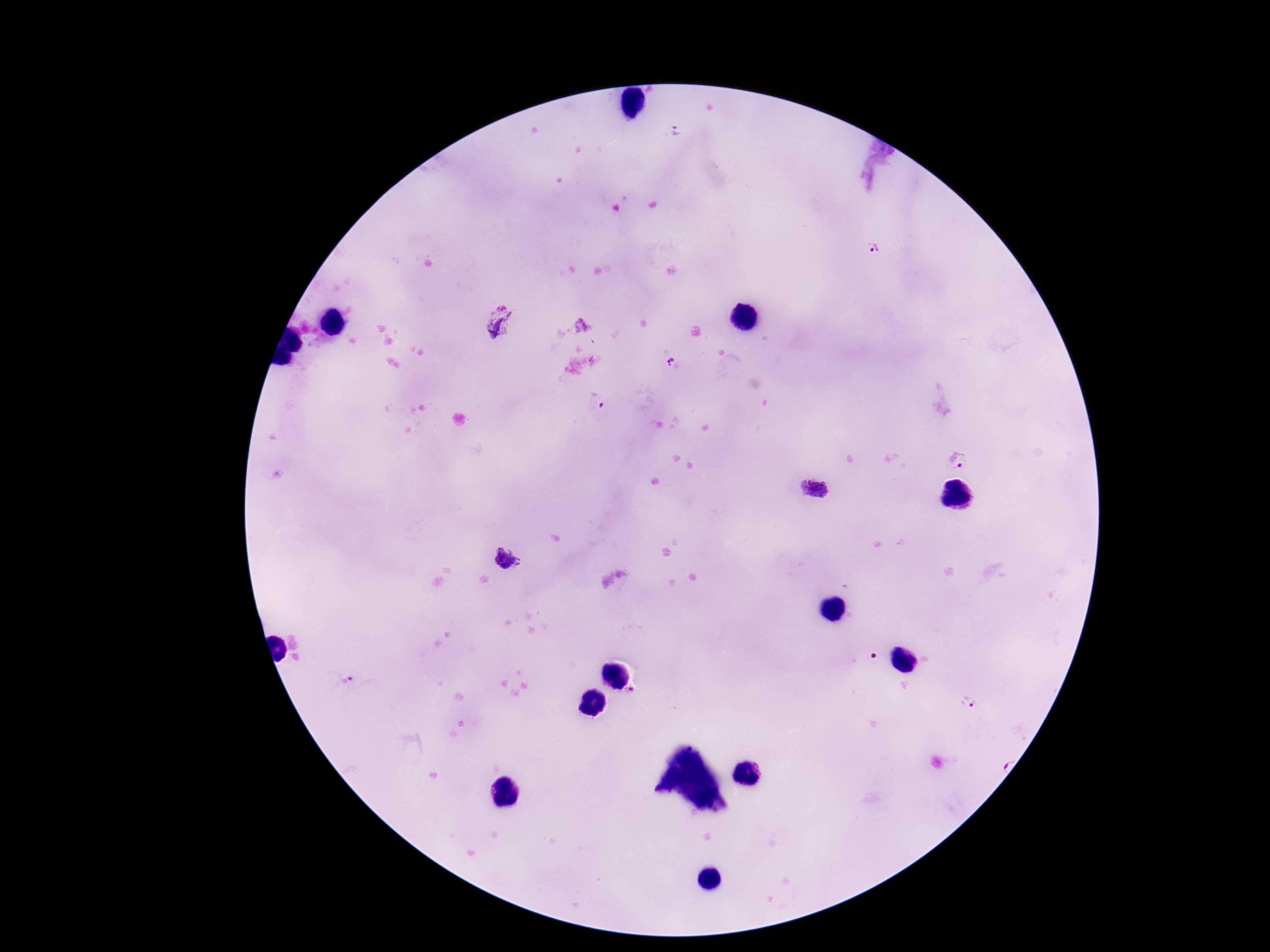
Approximate centers as (x, y) in pixels.
Summary:
  - Plasmodium parasite locations: (676, 131), (873, 248), (671, 359), (598, 401), (957, 459), (814, 489), (507, 558), (350, 681), (968, 700)
  - Capture: smartphone camera through the microscope eyepiece
  - Stain: Giemsa
  - Magnification: 100x
  - Image size: 1270×952 pixels
  - Field of view: single
  - Preparation: thick peripheral-blood smear
  - Patient malaria status: infected